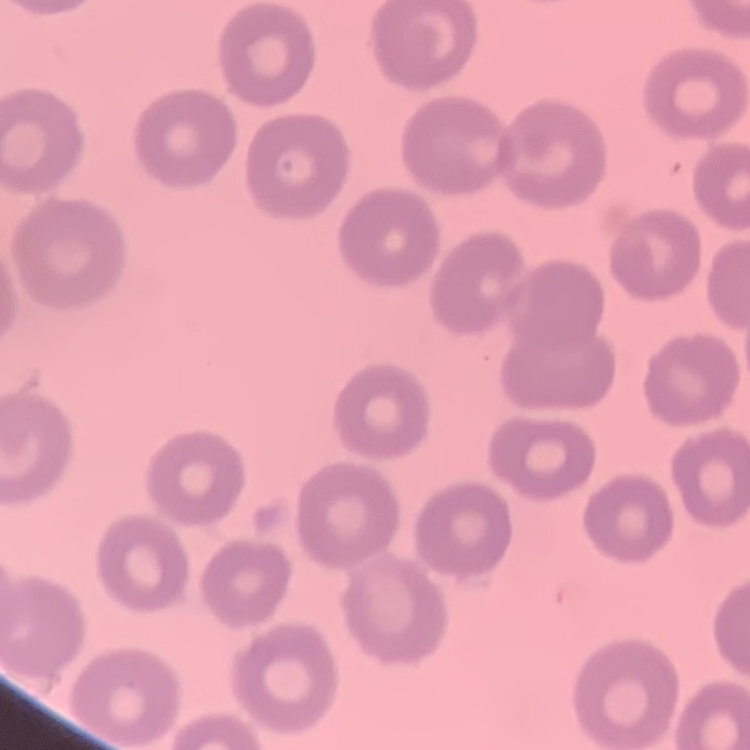
{
  "erythrocyte_morphology": "no rouleaux formation",
  "stain": "Field's or Giemsa",
  "image_type": "one tile cut from a larger photomicrograph",
  "preparation": "thin peripheral smear"
}